State the blood parasite species.
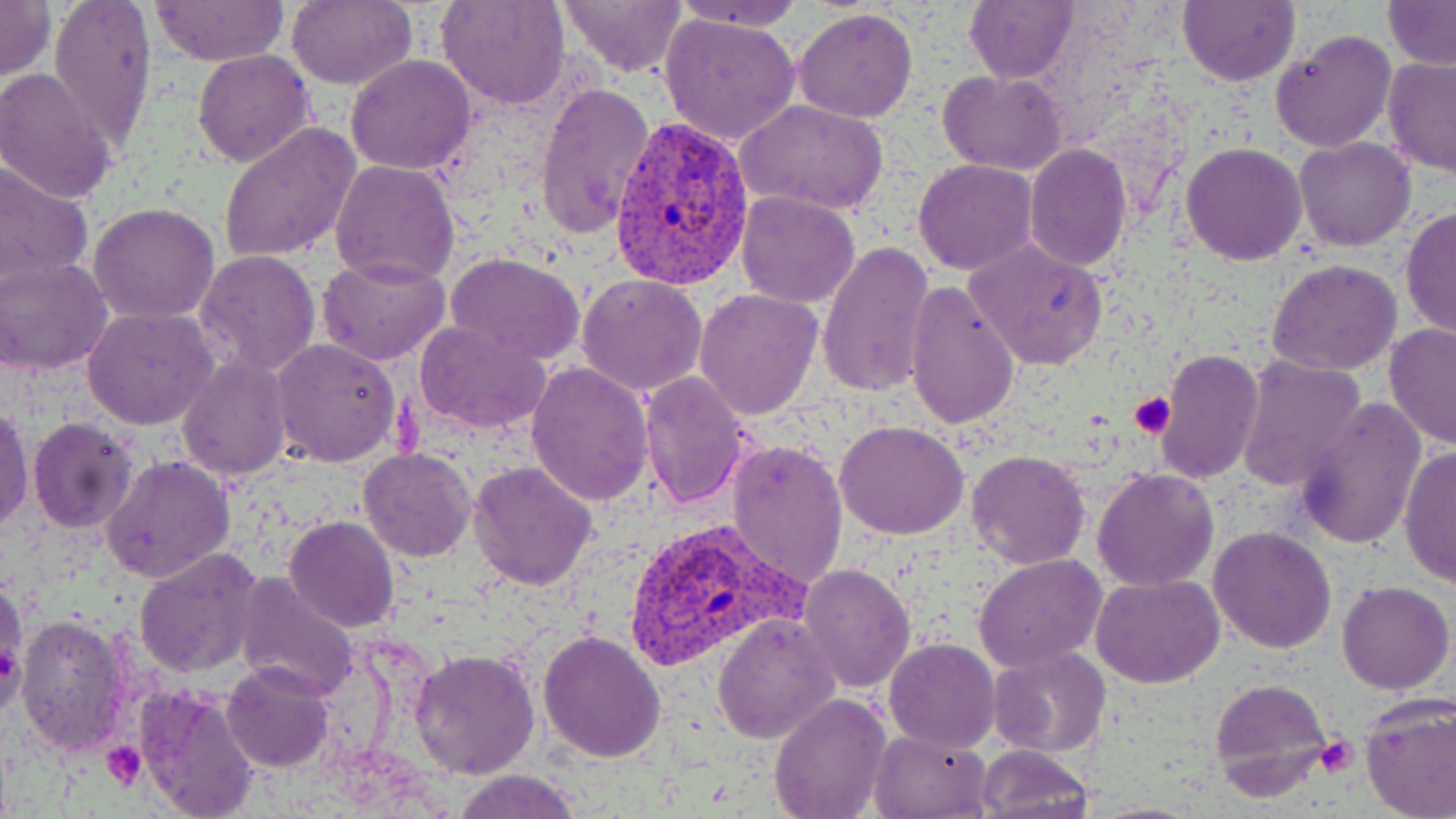
Plasmodium vivax.

{
  "field_of_view": "single",
  "platelet_locations": "approximate bounding boxes as (x1,y1)-(x2,y2) corner pairs in pixels: (1129,391)-(1177,437), (1314,735)-(1356,776), (102,742)-(145,789)",
  "plasmodium_vivax_infected_red_blood_cell_locations": "approximate bounding boxes as (x1,y1)-(x2,y2) corner pairs in pixels: (607,118)-(752,291), (624,514)-(802,674)",
  "preparation": "thin blood smear",
  "uninfected_red_blood_cell_locations": "approximate bounding boxes as (x1,y1)-(x2,y2) corner pairs in pixels: (0,0)-(54,85), (48,0)-(157,150), (149,0)-(288,66), (287,0)-(417,90), (438,0)-(569,110), (559,0)-(685,78), (963,0)-(1081,84), (1177,0)-(1299,87), (668,1)-(806,33), (1382,1)-(1456,70), (793,8)-(918,123), (658,11)-(803,147), (1269,28)-(1398,153), (193,49)-(316,168), (345,54)-(476,174), (1380,57)-(1456,176), (0,67)-(118,204), (939,69)-(1067,175), (534,81)-(656,237), (737,99)-(889,217), (217,124)-(362,265), (1295,137)-(1416,252), (1181,141)-(1307,265), (1023,143)-(1132,270), (329,158)-(459,288), (914,158)-(1037,274), (0,161)-(94,290), (735,191)-(861,309), (89,202)-(221,323), (1400,208)-(1456,341), (965,237)-(1109,370), (818,241)-(935,398), (195,249)-(322,381), (446,251)-(585,365), (319,256)-(451,366), (0,257)-(113,377), (1266,258)-(1401,376), (576,273)-(707,396), (904,282)-(1020,429), (694,288)-(822,420), (82,308)-(222,432), (412,320)-(553,436), (1384,322)-(1456,450), (272,338)-(400,466), (1158,349)-(1263,484), (176,355)-(291,481), (1237,356)-(1368,493), (526,363)-(655,505), (639,371)-(752,511), (1294,398)-(1426,549), (1,404)-(34,532), (28,417)-(138,532), (835,420)-(968,539), (725,439)-(849,589), (1397,444)-(1456,588), (358,447)-(478,563), (967,450)-(1090,569), (101,455)-(235,584), (469,460)-(598,590), (1093,467)-(1219,591), (283,516)-(400,633), (1207,525)-(1337,653), (132,547)-(263,678), (975,553)-(1107,671), (798,564)-(915,693), (1,574)-(26,715), (1089,575)-(1227,689), (233,577)-(361,705), (1336,579)-(1454,694), (14,611)-(133,755), (713,614)-(840,742), (539,628)-(669,763), (883,638)-(1000,753), (409,647)-(541,778), (989,648)-(1110,759), (220,661)-(333,771), (1207,678)-(1334,803), (137,685)-(258,818), (768,693)-(892,818), (1358,697)-(1456,819), (870,727)-(991,818), (975,744)-(1094,819), (447,769)-(585,819)",
  "modality": "optical microscopy",
  "image_size": "1456×819 pixels",
  "magnification": "1000x",
  "stain": "May-Grünwald-Giemsa"
}